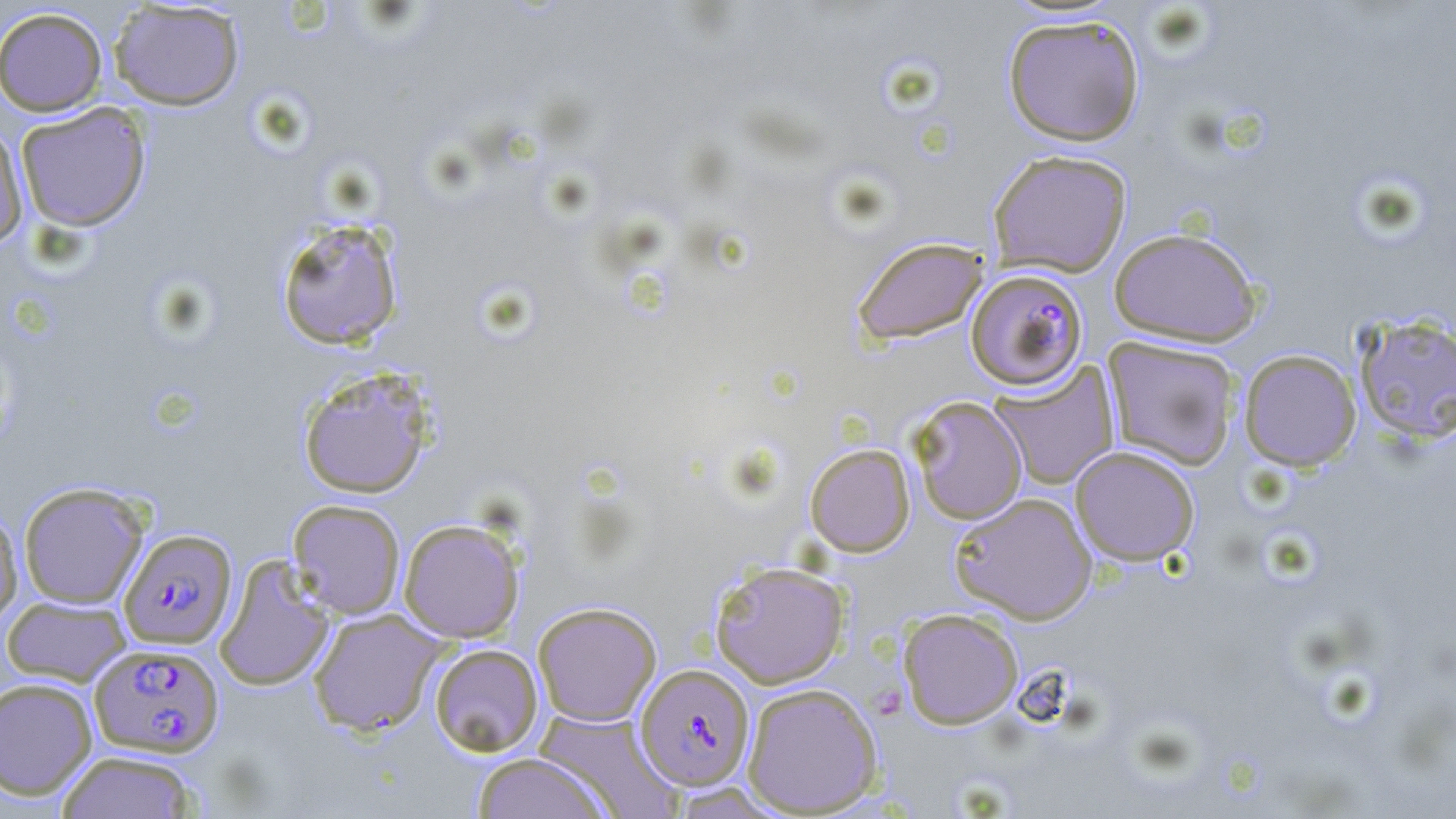
Approximate bounding boxes as (x1,y1)-(x2,y2) corner pairs in pixels. Plasmodium falciparum-infected red blood cell locations: (967,268)-(1088,390), (119,528)-(237,649), (89,642)-(224,758), (635,663)-(756,790). Uninfected red blood cell locations: (107,1)-(245,111), (0,7)-(108,116), (1002,13)-(1145,147), (15,103)-(151,232), (0,120)-(29,250), (988,149)-(1132,277), (274,217)-(405,351), (1108,227)-(1262,347), (851,236)-(988,347), (1353,312)-(1456,445), (1103,336)-(1241,471), (1238,349)-(1361,471), (990,363)-(1119,490), (297,366)-(436,499), (908,396)-(1028,524), (804,443)-(915,557), (1070,445)-(1201,566), (18,481)-(150,609), (949,491)-(1097,624), (287,499)-(406,619), (0,507)-(23,625), (399,518)-(525,643), (214,554)-(335,692), (709,559)-(850,688), (2,595)-(131,686), (532,601)-(662,726), (307,608)-(445,737), (897,608)-(1023,729), (429,643)-(543,757), (0,677)-(98,800), (742,682)-(883,816), (534,709)-(681,818), (57,750)-(199,819), (471,752)-(612,819). Slide-level diagnosis: Plasmodium falciparum. Captured at 1000x magnification. Thin blood smear. May-Grünwald-Giemsa-stained preparation. Image is 1456×819 pixels. Light microscopy. Single field of view.